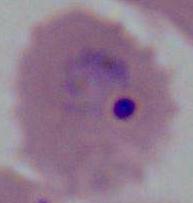

identification = Plasmodium
modality = photomicrograph
magnification = 400x or 1000x